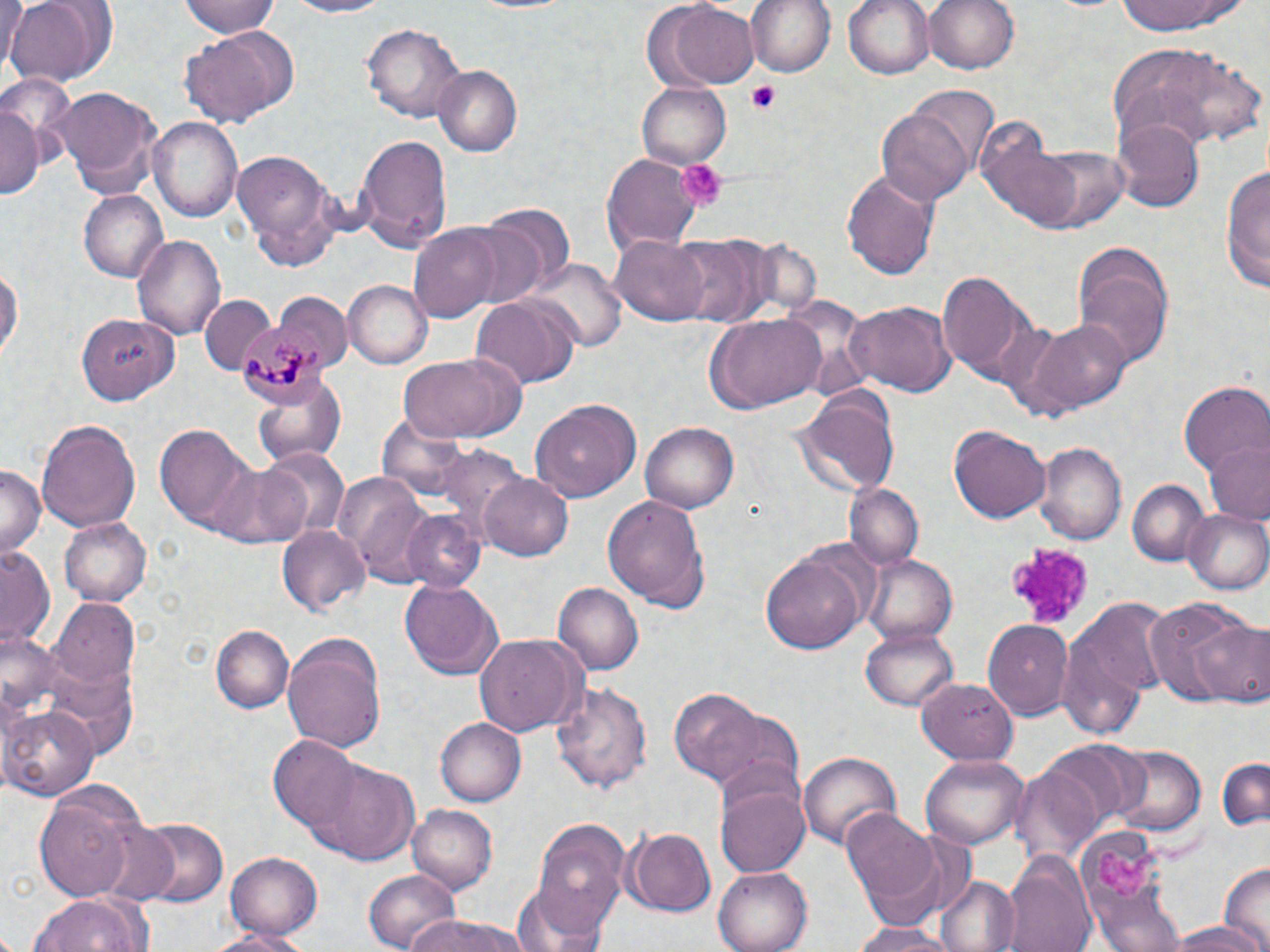

Approximate bounding boxes as named x1/y1/x2/y2 corners in pixels. Platelet locations: (x1=746, y1=80, x2=783, y2=114), (x1=678, y1=159, x2=728, y2=213), (x1=1002, y1=542, x2=1092, y2=631), (x1=1097, y1=846, x2=1160, y2=901). Plasmodium malariae-infected red blood cell locations: (x1=236, y1=321, x2=328, y2=410). Uninfected red blood cell locations: (x1=178, y1=0, x2=286, y2=38), (x1=281, y1=0, x2=399, y2=19), (x1=744, y1=0, x2=837, y2=78), (x1=844, y1=0, x2=937, y2=80), (x1=924, y1=0, x2=1020, y2=76), (x1=1112, y1=0, x2=1246, y2=36), (x1=1, y1=1, x2=30, y2=73), (x1=5, y1=1, x2=104, y2=87), (x1=182, y1=2, x2=287, y2=87), (x1=663, y1=2, x2=760, y2=89), (x1=363, y1=21, x2=467, y2=125), (x1=179, y1=27, x2=299, y2=124), (x1=1108, y1=43, x2=1261, y2=149), (x1=433, y1=66, x2=523, y2=155), (x1=639, y1=82, x2=731, y2=168), (x1=46, y1=85, x2=164, y2=200), (x1=911, y1=88, x2=1000, y2=181), (x1=1, y1=100, x2=40, y2=204), (x1=877, y1=106, x2=976, y2=206), (x1=149, y1=116, x2=243, y2=225), (x1=1114, y1=119, x2=1203, y2=210), (x1=972, y1=122, x2=1089, y2=231), (x1=355, y1=131, x2=450, y2=247), (x1=1038, y1=146, x2=1132, y2=232), (x1=231, y1=151, x2=342, y2=272), (x1=603, y1=156, x2=704, y2=254), (x1=1220, y1=165, x2=1269, y2=291), (x1=841, y1=169, x2=943, y2=281), (x1=79, y1=190, x2=166, y2=281), (x1=481, y1=203, x2=575, y2=298), (x1=408, y1=225, x2=504, y2=322), (x1=132, y1=232, x2=225, y2=338), (x1=670, y1=235, x2=764, y2=326), (x1=612, y1=236, x2=710, y2=324), (x1=1072, y1=256, x2=1172, y2=372), (x1=0, y1=259, x2=23, y2=369), (x1=531, y1=260, x2=624, y2=353), (x1=939, y1=272, x2=1032, y2=379), (x1=344, y1=280, x2=433, y2=369), (x1=275, y1=289, x2=351, y2=366), (x1=470, y1=294, x2=580, y2=388), (x1=841, y1=301, x2=957, y2=397), (x1=705, y1=314, x2=827, y2=415), (x1=77, y1=316, x2=176, y2=405), (x1=1012, y1=317, x2=1131, y2=418), (x1=398, y1=354, x2=523, y2=441), (x1=252, y1=378, x2=348, y2=466), (x1=1178, y1=381, x2=1268, y2=479), (x1=792, y1=384, x2=902, y2=498), (x1=532, y1=397, x2=642, y2=502), (x1=36, y1=417, x2=141, y2=531), (x1=641, y1=421, x2=739, y2=512), (x1=152, y1=423, x2=260, y2=534), (x1=949, y1=425, x2=1051, y2=524), (x1=1036, y1=441, x2=1127, y2=543), (x1=1206, y1=441, x2=1270, y2=523), (x1=430, y1=443, x2=524, y2=540), (x1=262, y1=446, x2=350, y2=541), (x1=209, y1=460, x2=315, y2=549), (x1=0, y1=464, x2=45, y2=557), (x1=335, y1=469, x2=443, y2=586), (x1=478, y1=471, x2=573, y2=562), (x1=1126, y1=478, x2=1209, y2=566), (x1=844, y1=482, x2=923, y2=571), (x1=604, y1=494, x2=712, y2=610), (x1=1183, y1=509, x2=1270, y2=596), (x1=400, y1=510, x2=488, y2=594), (x1=58, y1=517, x2=150, y2=605), (x1=277, y1=524, x2=370, y2=618), (x1=0, y1=543, x2=56, y2=652), (x1=761, y1=553, x2=869, y2=655), (x1=863, y1=554, x2=956, y2=645), (x1=401, y1=576, x2=505, y2=679), (x1=552, y1=583, x2=642, y2=674), (x1=52, y1=600, x2=140, y2=690), (x1=1143, y1=600, x2=1257, y2=707), (x1=1058, y1=609, x2=1160, y2=743), (x1=1188, y1=619, x2=1270, y2=707), (x1=983, y1=620, x2=1072, y2=720), (x1=211, y1=624, x2=292, y2=712), (x1=862, y1=628, x2=957, y2=710), (x1=474, y1=635, x2=585, y2=737), (x1=283, y1=636, x2=387, y2=751), (x1=42, y1=663, x2=138, y2=759), (x1=919, y1=679, x2=1020, y2=764), (x1=551, y1=680, x2=655, y2=795), (x1=668, y1=686, x2=773, y2=786), (x1=2, y1=705, x2=95, y2=799), (x1=703, y1=709, x2=809, y2=803), (x1=435, y1=718, x2=526, y2=805), (x1=268, y1=738, x2=360, y2=834), (x1=1036, y1=740, x2=1144, y2=836), (x1=1107, y1=743, x2=1208, y2=838), (x1=799, y1=750, x2=901, y2=853), (x1=923, y1=755, x2=1027, y2=848), (x1=1215, y1=756, x2=1269, y2=832), (x1=308, y1=759, x2=423, y2=863), (x1=1009, y1=765, x2=1103, y2=867), (x1=716, y1=781, x2=811, y2=877), (x1=33, y1=785, x2=149, y2=903), (x1=407, y1=805, x2=497, y2=892), (x1=840, y1=809, x2=947, y2=917), (x1=134, y1=817, x2=228, y2=908), (x1=528, y1=817, x2=632, y2=930), (x1=91, y1=820, x2=180, y2=907), (x1=622, y1=826, x2=717, y2=914), (x1=226, y1=851, x2=322, y2=941), (x1=1003, y1=852, x2=1097, y2=952), (x1=1218, y1=861, x2=1270, y2=951), (x1=714, y1=864, x2=816, y2=952), (x1=361, y1=868, x2=462, y2=952), (x1=935, y1=875, x2=1018, y2=952), (x1=513, y1=880, x2=616, y2=952), (x1=27, y1=891, x2=149, y2=952), (x1=401, y1=915, x2=532, y2=952), (x1=1159, y1=919, x2=1261, y2=950), (x1=848, y1=920, x2=955, y2=952), (x1=210, y1=926, x2=316, y2=952). Slide-level diagnosis: Plasmodium malariae. Thin blood film. 1000x magnification. Optical microscopy. May-Grünwald-Giemsa-stained preparation. Single field of view. Image is 1270×952 pixels.